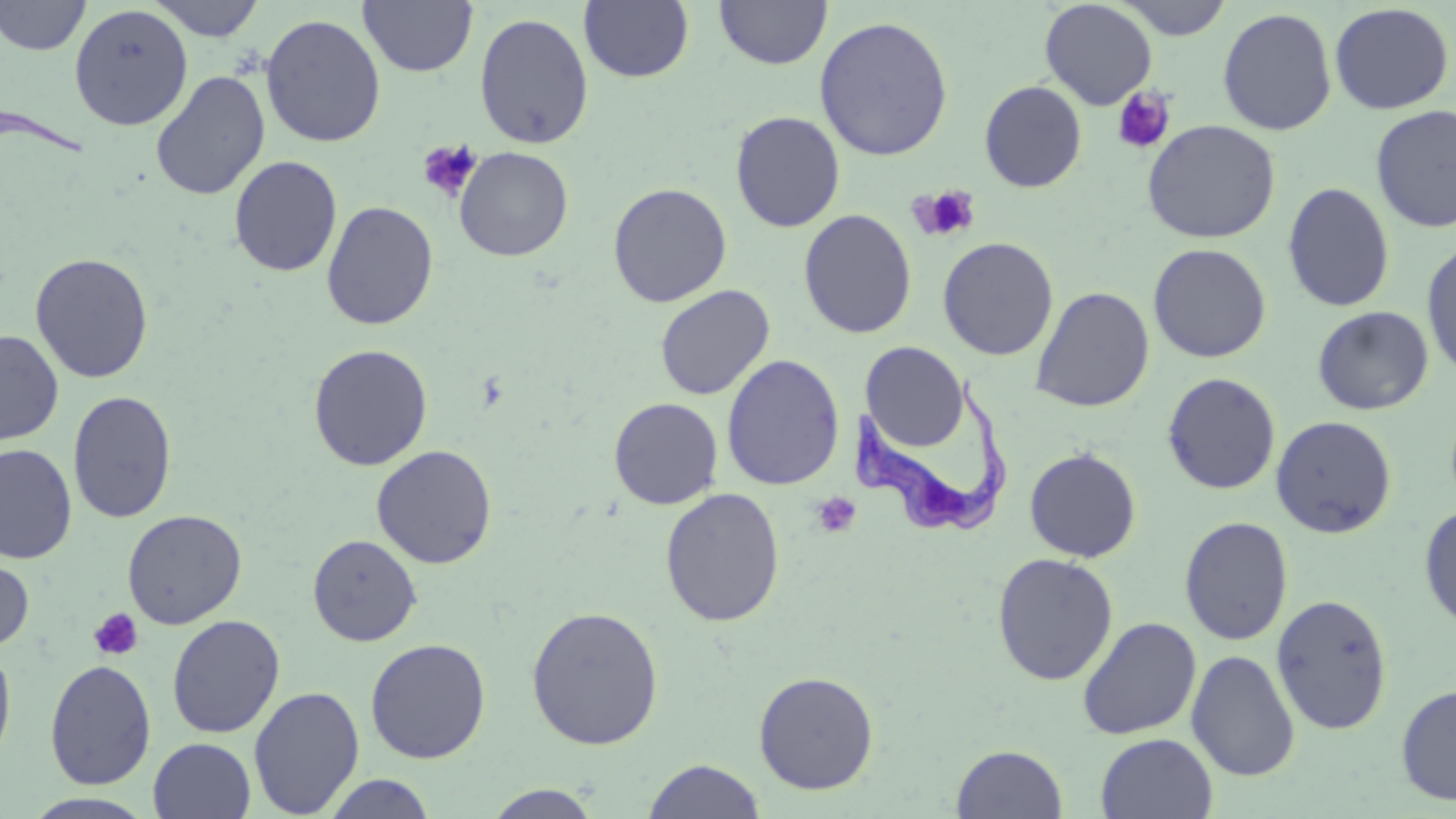
Approximate bounding boxes as [x1, y1, x2, y2] in pixels. Platelet locations: [1112, 86, 1175, 154], [417, 140, 483, 203], [910, 184, 981, 242], [811, 492, 863, 539], [88, 608, 144, 662]. Trypanosoma brucei locations: [0, 101, 90, 166], [850, 367, 1018, 543]. Uninfected red blood cell locations: [1, 0, 91, 56], [148, 0, 265, 41], [714, 0, 832, 69], [1039, 0, 1158, 110], [1116, 0, 1233, 40], [359, 1, 478, 76], [579, 1, 694, 84], [1328, 3, 1454, 115], [69, 5, 193, 131], [1217, 7, 1337, 136], [474, 10, 594, 151], [260, 13, 386, 148], [814, 15, 954, 161], [151, 70, 270, 201], [979, 80, 1087, 193], [1371, 104, 1456, 233], [730, 111, 846, 232], [1142, 119, 1281, 244], [454, 146, 573, 262], [229, 155, 343, 277], [608, 182, 732, 307], [1282, 182, 1395, 312], [322, 200, 439, 331], [798, 209, 917, 339], [938, 237, 1058, 360], [1421, 240, 1456, 381], [1157, 241, 1275, 493], [1148, 243, 1271, 363], [29, 252, 154, 383], [654, 285, 775, 401], [1030, 286, 1154, 412], [1312, 306, 1434, 415], [0, 330, 64, 445], [860, 342, 969, 451], [307, 344, 433, 471], [721, 354, 845, 491], [1161, 372, 1281, 495], [67, 390, 177, 524], [609, 397, 724, 509], [1270, 415, 1397, 538], [0, 444, 77, 563], [371, 444, 497, 568], [1024, 447, 1142, 562], [660, 488, 785, 627], [1418, 504, 1456, 632], [122, 509, 247, 629], [1179, 516, 1293, 646], [307, 534, 422, 647], [992, 552, 1118, 685], [0, 554, 35, 653], [1271, 593, 1393, 735], [526, 606, 664, 750], [166, 614, 285, 739], [1077, 616, 1202, 740], [365, 638, 491, 763], [0, 639, 17, 770], [1186, 649, 1300, 781], [44, 659, 157, 789], [753, 671, 879, 795], [1396, 683, 1456, 807], [248, 685, 365, 817], [1095, 733, 1218, 818], [148, 737, 256, 819], [951, 744, 1068, 818], [642, 758, 767, 818], [321, 773, 438, 818], [483, 784, 604, 819], [20, 792, 159, 819]. Slide-level diagnosis: Trypanosoma brucei. May-Grünwald-Giemsa stain. One field of a larger specimen. Image is 1456×819 pixels. 1000x magnification. Thin blood film. Optical microscopy.